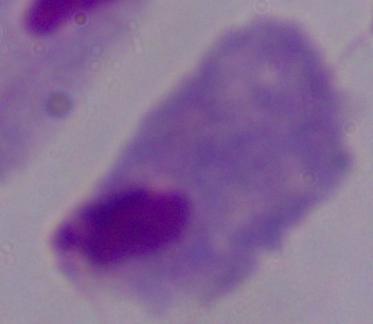

Photomicrograph. A trichomonad is seen. 1000x magnification.